Assess this cell for malaria.
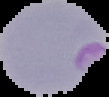
It is parasitized.

Image is 109×97 pixels. The area outside the segmented cell region is set to black. From a thin blood smear.